Give the position of every malaria parasite.
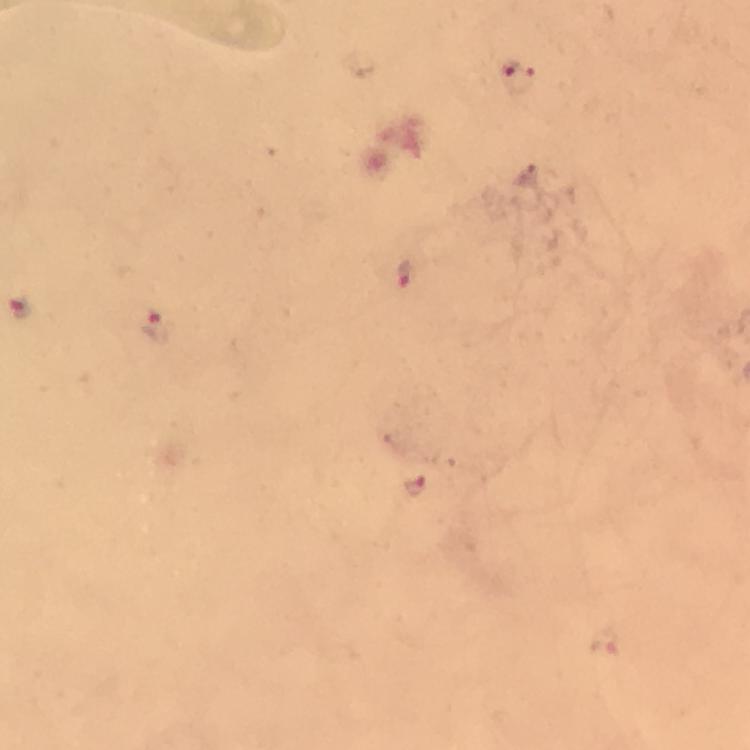
Approximate centers as [x, y] in pixels.
Malaria parasites: [516, 78], [404, 273], [21, 304], [153, 328], [414, 485].

preparation = thick blood film
cropped from = a single field of view
image size = 750×750 pixels
capture = smartphone mounted on the microscope
stain = Giemsa
context = from a malaria diagnostic workup
immersion oil = used
magnification = 100x